Report the malaria status of this cell.
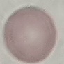
It is uninfected.

image type = cell patch, automatically extracted from a larger field of view and resized to 64 × 64 pixels
capture = smartphone camera at the microscope eyepiece
stain = Giemsa
preparation = thin smear